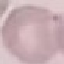

Summary:
  - Result: no malaria parasites seen
  - Image type: cell patch, automatically extracted from a larger field of view and resized to 64 × 64 pixels
  - Preparation: thin blood smear
  - Stain: Giemsa
  - Capture: smartphone through the microscope eyepiece